Comment on the morphology of the erythrocytes.
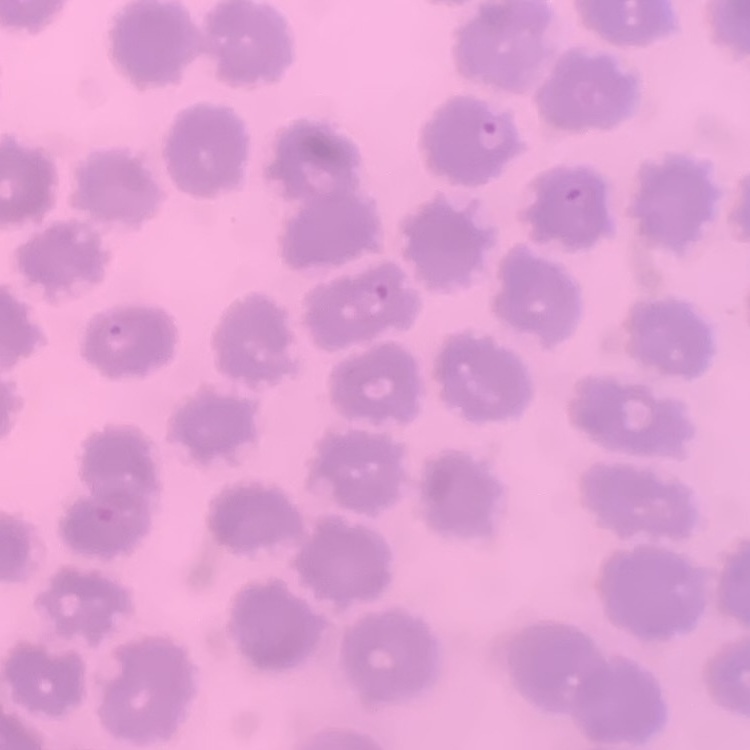

No rouleaux formation.

Thin peripheral smear. Square crop of a larger photomicrograph. Field's or Giemsa stain.